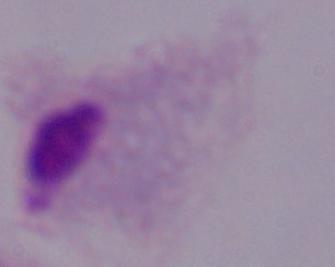
{
  "modality": "photomicrograph",
  "magnification": "1000x",
  "identification": "trichomonad"
}